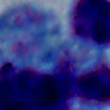

A leukocyte is seen. Photomicrograph. Captured at 1000x magnification.